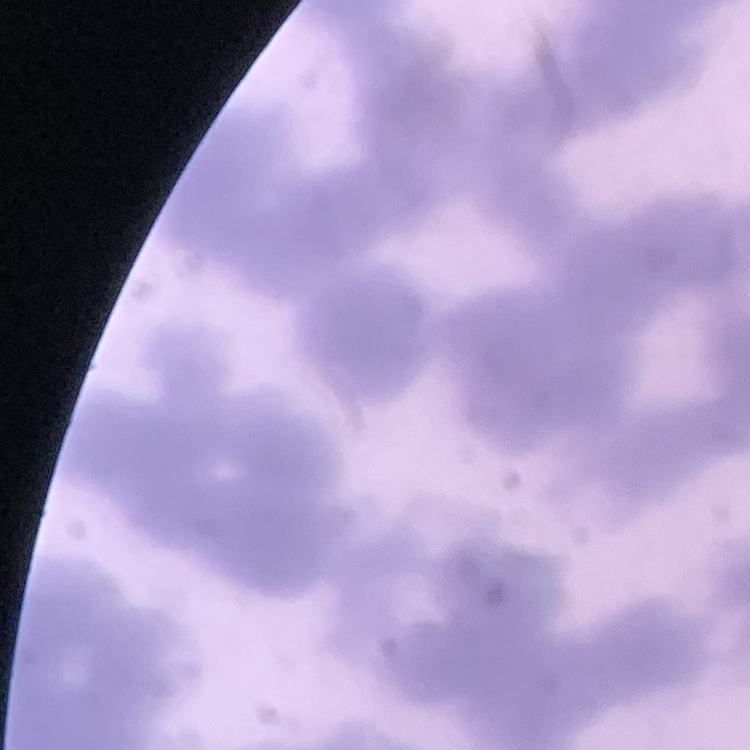
Summary:
  - Red blood cell morphology: rouleaux formation
  - Stain: Field's or Giemsa
  - Preparation: thin blood film
  - Image type: one tile cut from a larger photomicrograph